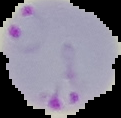

Summary:
  - Result: Plasmodium parasites identified
  - Preparation: thin blood film
  - Image size: 121×118 pixels
  - Image type: cell region segmented out of the field of view; surrounding area masked to black